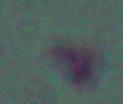

Summary:
  - Modality: photomicrograph
  - Identification: Leishmania
  - Magnification: 1000x